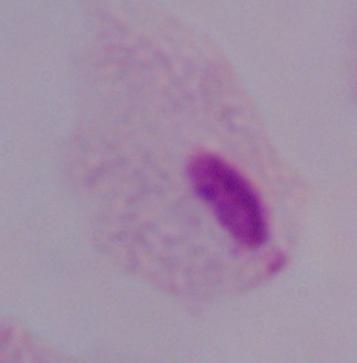

Photomicrograph. 1000x magnification. A trichomonad is seen.